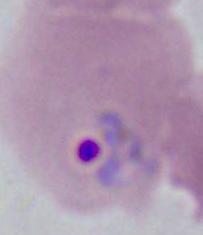

{
  "identification": "Plasmodium",
  "modality": "photomicrograph",
  "magnification": "400x or 1000x"
}